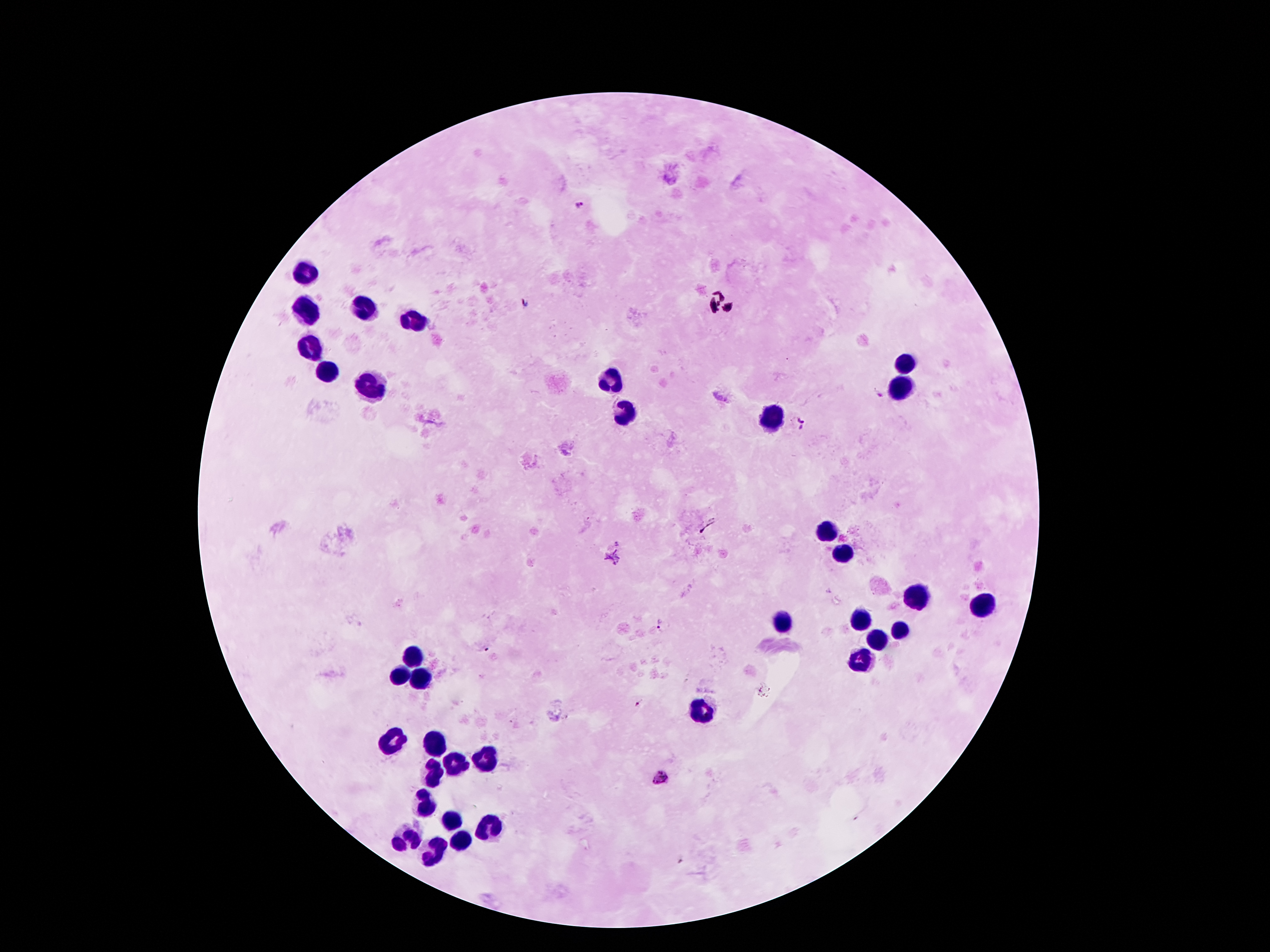
Approximate centers as (x, y) in pixels. Plasmodium parasite locations: (578, 205), (525, 304), (878, 392), (796, 424), (660, 624), (638, 703), (660, 778). Leukocyte locations: (308, 271), (360, 308), (306, 310), (408, 319), (312, 349), (905, 366), (328, 373), (610, 380), (369, 387), (903, 389), (622, 410), (767, 417), (823, 532), (841, 553), (916, 598), (985, 603), (782, 623), (860, 623), (901, 630), (878, 637), (412, 657), (860, 662), (403, 676), (419, 680), (703, 714), (390, 741), (437, 746), (481, 758), (456, 762), (433, 775), (424, 803), (449, 817), (487, 828), (458, 841), (404, 842), (431, 850). One field from this slide. Thick peripheral-blood smear. Giemsa-stained preparation. Patient malaria status: infected with Plasmodium falciparum. 100x magnification. Smartphone photograph taken through the microscope eyepiece. Image is 1270×952 pixels.